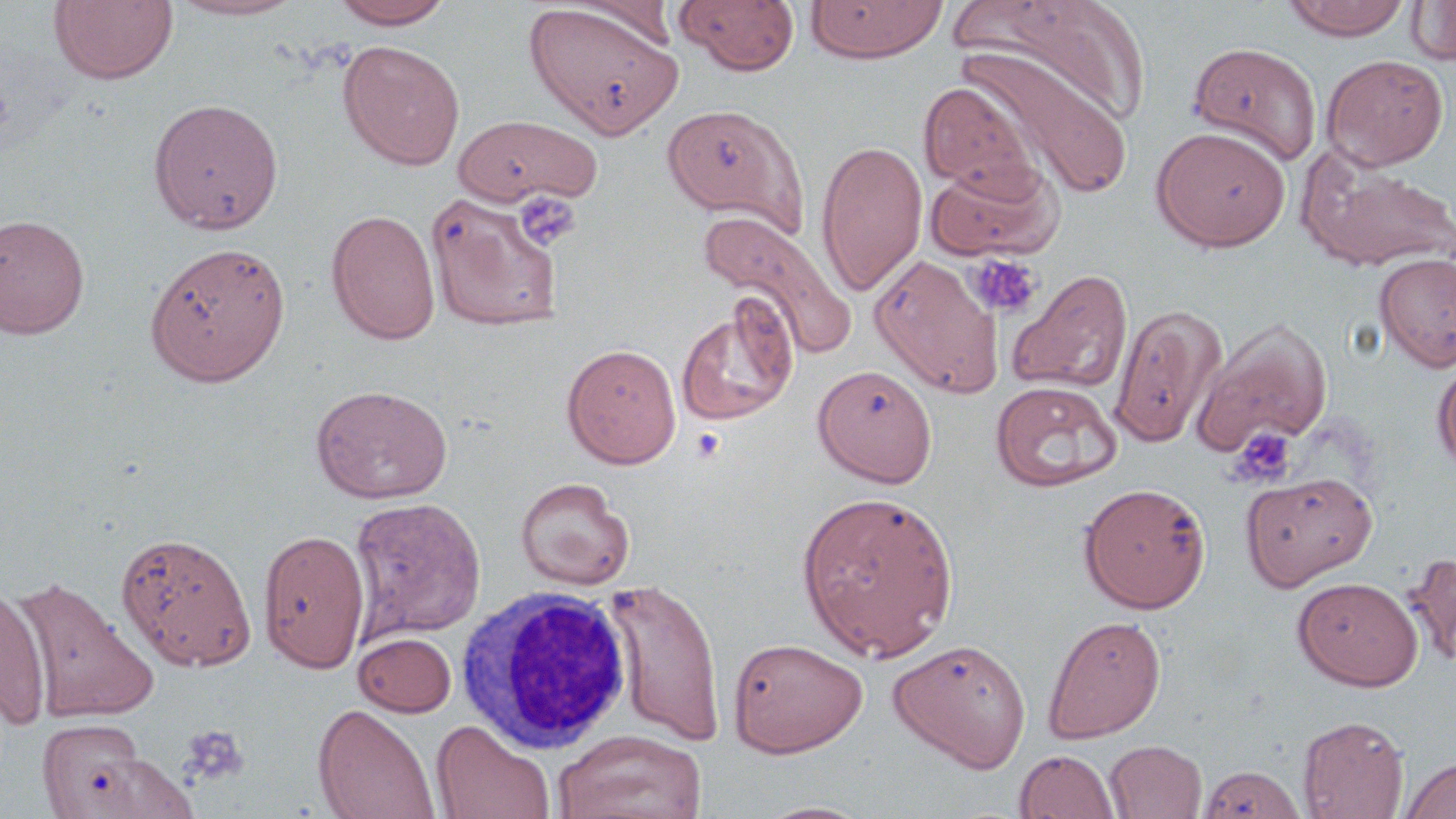
slide-level diagnosis = negative for blood parasites
platelet locations = approximate bounding boxes as (x1, y1, x2, y2) in pixels: (514, 191, 582, 251), (965, 253, 1042, 319), (1229, 425, 1296, 486), (180, 725, 250, 787)
uninfected red blood cell locations = approximate bounding boxes as (x1, y1, x2, y2) in pixels: (166, 0, 308, 21), (330, 0, 456, 29), (674, 0, 801, 76), (805, 0, 948, 64), (953, 0, 1150, 129), (1283, 0, 1413, 40), (48, 1, 179, 85), (567, 1, 682, 50), (1406, 1, 1456, 66), (524, 2, 683, 139), (338, 40, 465, 170), (1188, 41, 1323, 166), (959, 47, 1134, 201), (1321, 53, 1449, 170), (918, 82, 1042, 197), (148, 97, 284, 234), (662, 103, 807, 228), (452, 113, 601, 208), (1150, 126, 1291, 251), (815, 138, 927, 297), (1298, 151, 1456, 274), (924, 158, 1064, 261), (425, 190, 564, 331), (326, 210, 441, 345), (701, 210, 856, 360), (0, 214, 90, 339), (145, 242, 290, 386), (1374, 252, 1456, 371), (870, 255, 1002, 396), (1006, 268, 1132, 395), (677, 300, 799, 425), (1110, 302, 1227, 448), (1192, 317, 1333, 457), (561, 343, 682, 468), (1432, 356, 1456, 477), (812, 363, 938, 487), (990, 380, 1122, 491), (311, 384, 452, 504), (1241, 469, 1377, 591), (515, 477, 635, 590), (1078, 481, 1212, 613), (796, 489, 959, 660), (350, 498, 486, 641), (258, 528, 371, 674), (116, 531, 256, 671), (1402, 550, 1456, 668), (10, 575, 159, 722), (1292, 576, 1424, 690), (604, 578, 727, 747), (0, 585, 52, 729), (1042, 614, 1167, 743), (354, 632, 457, 717), (728, 637, 868, 757), (888, 638, 1031, 772), (312, 702, 441, 819), (1297, 715, 1409, 818), (37, 719, 152, 817), (431, 719, 556, 819), (553, 729, 709, 819), (1104, 740, 1207, 818), (1014, 749, 1120, 818), (76, 751, 200, 818), (1400, 756, 1456, 819), (1196, 762, 1308, 819), (753, 800, 875, 819)
magnification = 1000x
stain = May-Grünwald-Giemsa
field of view = single
white blood cell locations = approximate bounding boxes as (x1, y1, x2, y2) in pixels: (457, 586, 635, 753)
preparation = thin blood film
modality = optical microscopy
image size = 1456×819 pixels